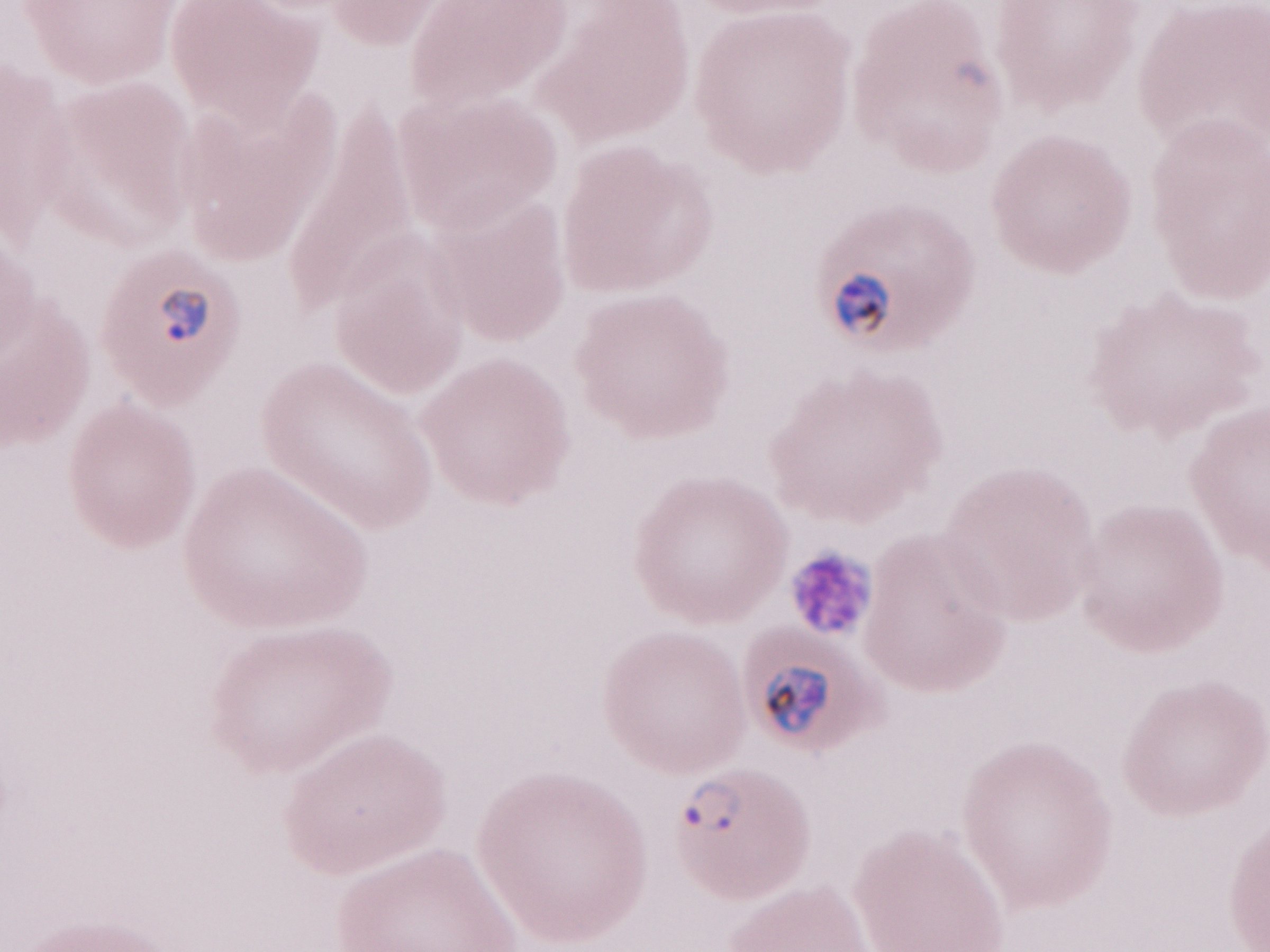 Thin peripheral-blood smear. Olympus BX43 microscope, Olympus DP73 camera. Patient diagnosis: malaria infection. May-Grünwald-Giemsa (MGG) stain. 1,000x magnification. Image is 1270×952 pixels. One field of this slide.